Locate and identify every blood parasite.
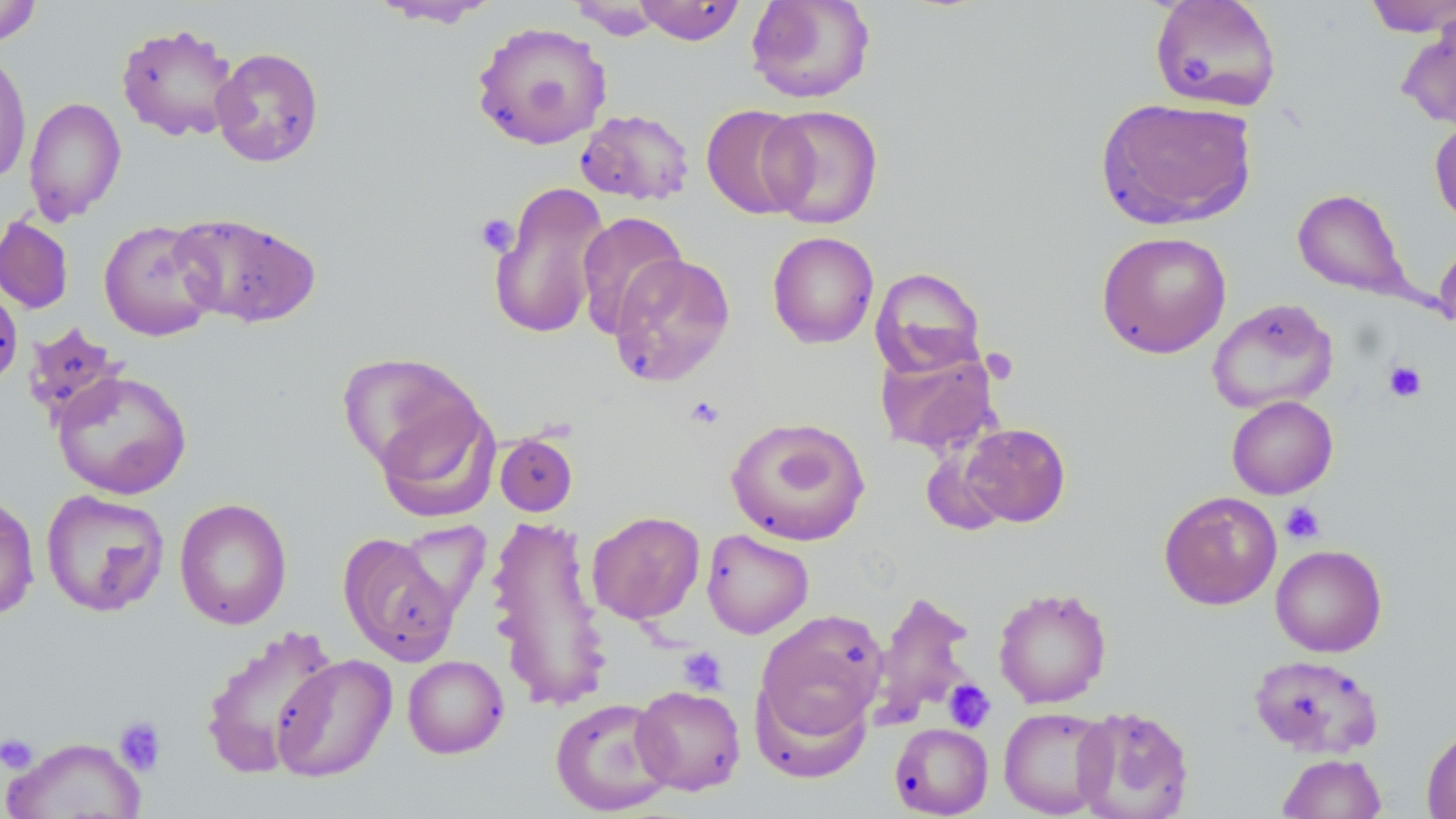

No blood parasites seen.

Summary:
  - Coordinate format: approximate bounding boxes as named x1/y1/x2/y2 corners in pixels
  - Uninfected red blood cell locations: (x1=632, y1=0, x2=746, y2=45), (x1=745, y1=0, x2=877, y2=104), (x1=1149, y1=0, x2=1282, y2=112), (x1=1361, y1=0, x2=1456, y2=37), (x1=0, y1=1, x2=43, y2=48), (x1=368, y1=1, x2=501, y2=28), (x1=570, y1=1, x2=664, y2=40), (x1=1397, y1=10, x2=1456, y2=131), (x1=472, y1=21, x2=612, y2=150), (x1=116, y1=22, x2=240, y2=142), (x1=210, y1=47, x2=324, y2=168), (x1=0, y1=51, x2=32, y2=185), (x1=23, y1=96, x2=127, y2=225), (x1=1096, y1=96, x2=1258, y2=229), (x1=701, y1=104, x2=811, y2=219), (x1=760, y1=104, x2=884, y2=229), (x1=575, y1=109, x2=695, y2=205), (x1=1430, y1=117, x2=1456, y2=229), (x1=488, y1=179, x2=612, y2=341), (x1=1292, y1=187, x2=1414, y2=301), (x1=169, y1=211, x2=321, y2=329), (x1=575, y1=211, x2=688, y2=338), (x1=0, y1=215, x2=75, y2=315), (x1=98, y1=219, x2=220, y2=341), (x1=1096, y1=230, x2=1232, y2=359), (x1=767, y1=231, x2=879, y2=348), (x1=1433, y1=241, x2=1456, y2=332), (x1=608, y1=253, x2=736, y2=387), (x1=870, y1=267, x2=986, y2=377), (x1=0, y1=280, x2=23, y2=390), (x1=1207, y1=298, x2=1339, y2=415), (x1=22, y1=322, x2=127, y2=427), (x1=874, y1=345, x2=1001, y2=456), (x1=337, y1=352, x2=484, y2=476), (x1=51, y1=370, x2=193, y2=500), (x1=1226, y1=395, x2=1338, y2=499), (x1=374, y1=398, x2=498, y2=523), (x1=725, y1=416, x2=871, y2=547), (x1=958, y1=422, x2=1071, y2=528), (x1=495, y1=432, x2=578, y2=516), (x1=39, y1=489, x2=170, y2=618), (x1=1158, y1=490, x2=1282, y2=611), (x1=0, y1=492, x2=40, y2=622), (x1=174, y1=497, x2=292, y2=630), (x1=587, y1=510, x2=705, y2=625), (x1=485, y1=513, x2=612, y2=713), (x1=394, y1=520, x2=491, y2=618), (x1=701, y1=529, x2=814, y2=639), (x1=338, y1=532, x2=462, y2=665), (x1=1270, y1=544, x2=1387, y2=657), (x1=993, y1=587, x2=1112, y2=708), (x1=868, y1=590, x2=978, y2=728), (x1=755, y1=610, x2=888, y2=742), (x1=200, y1=625, x2=340, y2=777), (x1=1250, y1=653, x2=1384, y2=759), (x1=271, y1=654, x2=397, y2=782), (x1=402, y1=655, x2=509, y2=759), (x1=754, y1=681, x2=872, y2=782), (x1=631, y1=684, x2=746, y2=795), (x1=549, y1=697, x2=676, y2=815), (x1=1072, y1=705, x2=1195, y2=819), (x1=998, y1=706, x2=1115, y2=818), (x1=890, y1=722, x2=993, y2=818), (x1=1421, y1=725, x2=1456, y2=819), (x1=1, y1=736, x2=147, y2=818), (x1=1278, y1=752, x2=1386, y2=818)
  - Platelet locations: (x1=1178, y1=55, x2=1213, y2=88), (x1=474, y1=213, x2=520, y2=256), (x1=1383, y1=360, x2=1427, y2=403), (x1=684, y1=395, x2=725, y2=429), (x1=1280, y1=502, x2=1325, y2=544), (x1=678, y1=647, x2=727, y2=695), (x1=943, y1=679, x2=995, y2=732), (x1=113, y1=715, x2=167, y2=777), (x1=0, y1=733, x2=39, y2=774)
  - Slide-level diagnosis: negative for blood parasites
  - Modality: light microscopy
  - Image size: 1456×819 pixels
  - Preparation: thin blood film
  - Magnification: 1000x
  - Stain: May-Grünwald-Giemsa
  - Field of view: single